State which parasite is depicted.
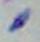

This is Toxoplasma gondii.

Summary:
  - Magnification: 1000x
  - Modality: photomicrograph